Classify this cell by malaria status.
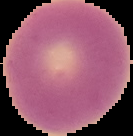
It is uninfected.

Summary:
  - Image size: 133×136 pixels
  - Image type: cell region segmented out of the field of view; surrounding area masked to black
  - Preparation: thin blood film